Report the malaria status of this cell.
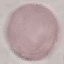
It is uninfected.

{
  "preparation": "thin smear",
  "stain": "Giemsa",
  "image_type": "cell patch, automatically extracted from a larger field of view and resized to 64 × 64 pixels",
  "capture": "smartphone camera at the microscope eyepiece"
}